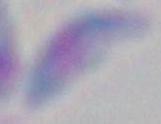
Photomicrograph. Toxoplasma gondii is shown. Captured at 1000x magnification.